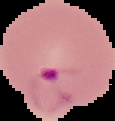

From a thin blood smear. The area outside the segmented cell region is set to black. Image is 115×121 pixels. Result: Plasmodium parasites identified.